Locate and identify every blood parasite.
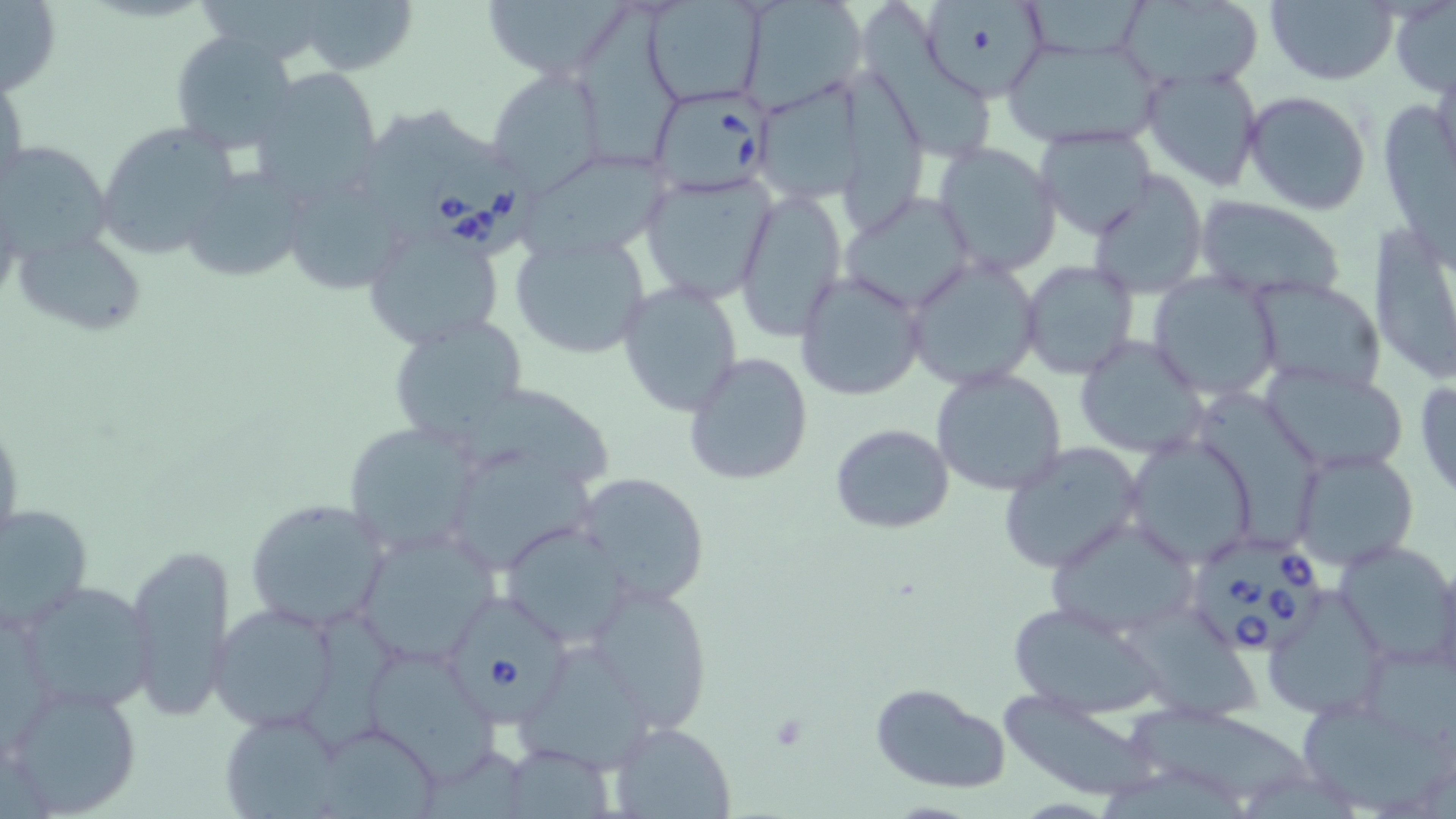

Approximate bounding boxes as named x1/y1/x2/y2 corners in pixels.
Babesia divergens-infected red blood cells: (x1=647, y1=87, x2=771, y2=194), (x1=428, y1=155, x2=548, y2=259), (x1=1198, y1=542, x2=1325, y2=662), (x1=454, y1=597, x2=577, y2=729).
No Plasmodium falciparum, Plasmodium ovale, Plasmodium malariae, Plasmodium vivax, or Trypanosoma brucei observed.

Uninfected red blood cell locations: (x1=0, y1=0, x2=61, y2=98), (x1=293, y1=0, x2=419, y2=77), (x1=477, y1=0, x2=634, y2=83), (x1=643, y1=0, x2=766, y2=109), (x1=738, y1=0, x2=868, y2=110), (x1=1113, y1=0, x2=1266, y2=91), (x1=1390, y1=0, x2=1456, y2=97), (x1=1027, y1=1, x2=1157, y2=51), (x1=1265, y1=1, x2=1397, y2=85), (x1=862, y1=2, x2=994, y2=165), (x1=925, y1=3, x2=1048, y2=100), (x1=580, y1=9, x2=686, y2=173), (x1=170, y1=31, x2=302, y2=154), (x1=1001, y1=34, x2=1164, y2=150), (x1=1140, y1=64, x2=1263, y2=192), (x1=483, y1=67, x2=607, y2=195), (x1=838, y1=68, x2=927, y2=236), (x1=0, y1=69, x2=27, y2=201), (x1=254, y1=70, x2=381, y2=202), (x1=765, y1=81, x2=865, y2=208), (x1=1242, y1=91, x2=1372, y2=215), (x1=1386, y1=104, x2=1456, y2=273), (x1=362, y1=109, x2=488, y2=242), (x1=95, y1=120, x2=241, y2=262), (x1=1035, y1=128, x2=1157, y2=240), (x1=2, y1=141, x2=114, y2=265), (x1=934, y1=142, x2=1062, y2=275), (x1=521, y1=158, x2=675, y2=259), (x1=185, y1=169, x2=316, y2=284), (x1=639, y1=170, x2=779, y2=305), (x1=1087, y1=172, x2=1208, y2=298), (x1=292, y1=181, x2=416, y2=300), (x1=734, y1=188, x2=848, y2=342), (x1=839, y1=191, x2=978, y2=315), (x1=1192, y1=197, x2=1347, y2=304), (x1=1371, y1=222, x2=1456, y2=386), (x1=361, y1=224, x2=504, y2=350), (x1=15, y1=229, x2=149, y2=335), (x1=509, y1=232, x2=651, y2=360), (x1=903, y1=256, x2=1040, y2=390), (x1=1019, y1=259, x2=1141, y2=382), (x1=795, y1=271, x2=926, y2=402), (x1=1148, y1=272, x2=1283, y2=401), (x1=1248, y1=276, x2=1388, y2=396), (x1=617, y1=283, x2=743, y2=417), (x1=386, y1=314, x2=530, y2=449), (x1=1072, y1=334, x2=1210, y2=458), (x1=684, y1=350, x2=815, y2=487), (x1=1261, y1=364, x2=1409, y2=475), (x1=931, y1=367, x2=1068, y2=497), (x1=1415, y1=374, x2=1456, y2=499), (x1=470, y1=389, x2=619, y2=490), (x1=1195, y1=395, x2=1327, y2=550), (x1=341, y1=421, x2=482, y2=559), (x1=829, y1=422, x2=955, y2=534), (x1=1122, y1=434, x2=1260, y2=569), (x1=998, y1=441, x2=1146, y2=575), (x1=1290, y1=447, x2=1419, y2=570), (x1=452, y1=454, x2=608, y2=568), (x1=574, y1=471, x2=710, y2=608), (x1=245, y1=498, x2=388, y2=629), (x1=0, y1=502, x2=94, y2=634), (x1=1044, y1=516, x2=1200, y2=641), (x1=497, y1=523, x2=635, y2=647), (x1=350, y1=529, x2=506, y2=667), (x1=1333, y1=539, x2=1456, y2=669), (x1=125, y1=541, x2=236, y2=722), (x1=588, y1=582, x2=714, y2=730), (x1=32, y1=586, x2=161, y2=716), (x1=1261, y1=590, x2=1400, y2=726), (x1=1006, y1=601, x2=1162, y2=717), (x1=208, y1=603, x2=337, y2=732), (x1=300, y1=606, x2=401, y2=757), (x1=1133, y1=607, x2=1272, y2=728), (x1=1356, y1=637, x2=1454, y2=748), (x1=519, y1=647, x2=660, y2=775), (x1=365, y1=651, x2=500, y2=785), (x1=7, y1=682, x2=143, y2=816), (x1=867, y1=682, x2=1011, y2=796), (x1=997, y1=693, x2=1158, y2=799), (x1=1125, y1=704, x2=1311, y2=801), (x1=1303, y1=710, x2=1456, y2=807), (x1=221, y1=711, x2=343, y2=817), (x1=610, y1=720, x2=736, y2=818), (x1=324, y1=724, x2=452, y2=819). Slide-level diagnosis: Babesia divergens. May-Grünwald-Giemsa-stained preparation. Captured at 1000x magnification. Thin blood film. One field of a larger specimen. Light microscopy. Image is 1456×819 pixels.